State which parasite is depicted.
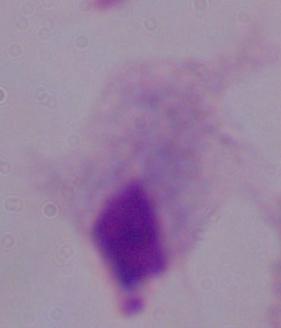

This is a trichomonad.

1000x magnification. Micrograph.